Assess this cell for malaria.
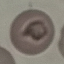

It is uninfected.

Cell patch, automatically extracted from a larger field of view and resized to 64 × 64 pixels. Acquired by smartphone through the microscope eyepiece. Thin blood smear. Giemsa-stained preparation.